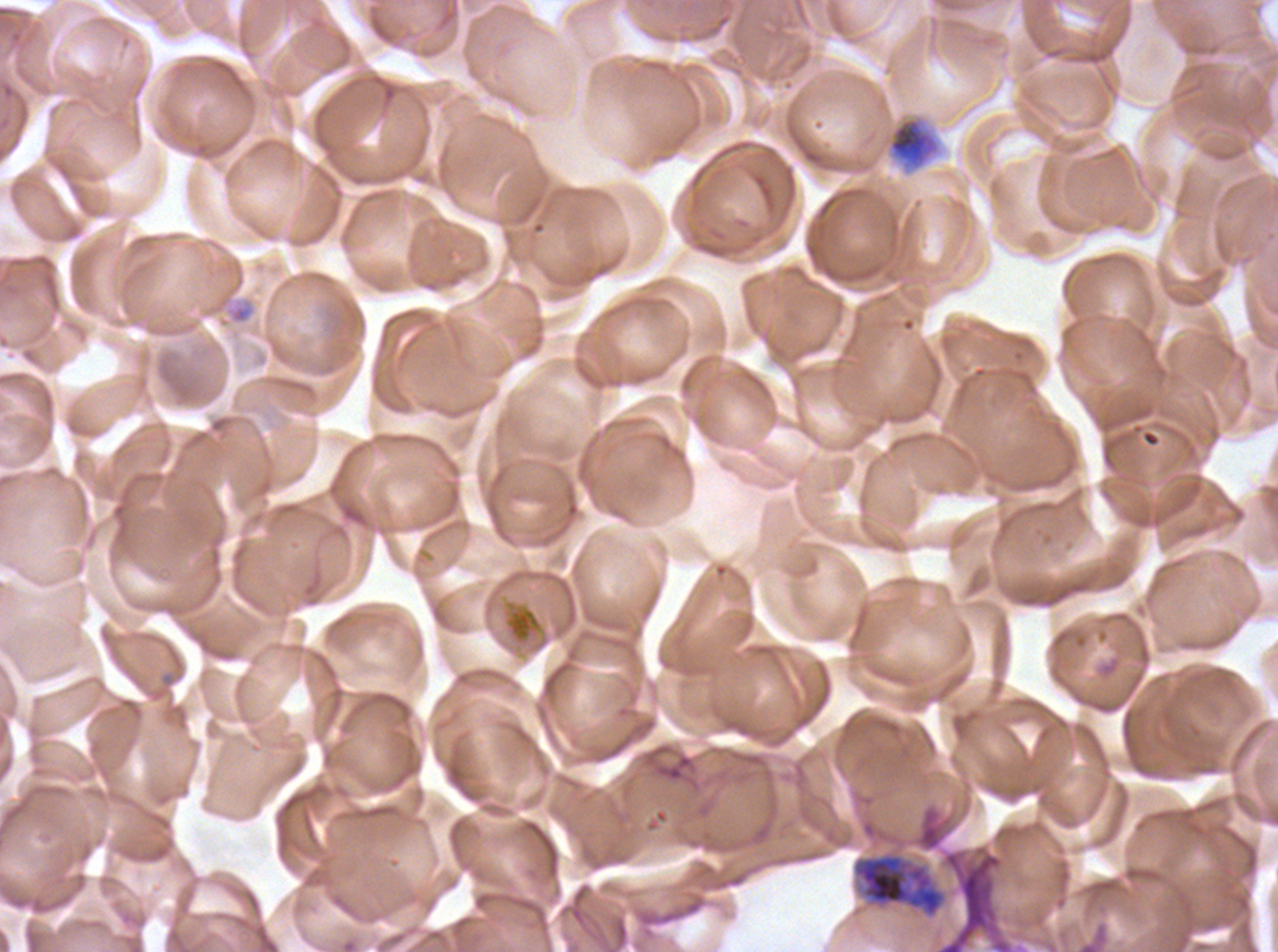

Approximate bounding rectangles given as corner coordinates in pixels from the top-left.
Summary:
  - Late schizont locations: (x1=851, y1=849, x2=949, y2=920)
  - Specimen: Plasmodium falciparum cultured ex vivo for 24 to 48 hours, from a patient in The Gambia
  - Field of view: one sub-image of a larger composite
  - Stain: Giemsa
  - Image size: 1278×952 pixels
  - Preparation: thin blood film